Point out each Plasmodium parasite.
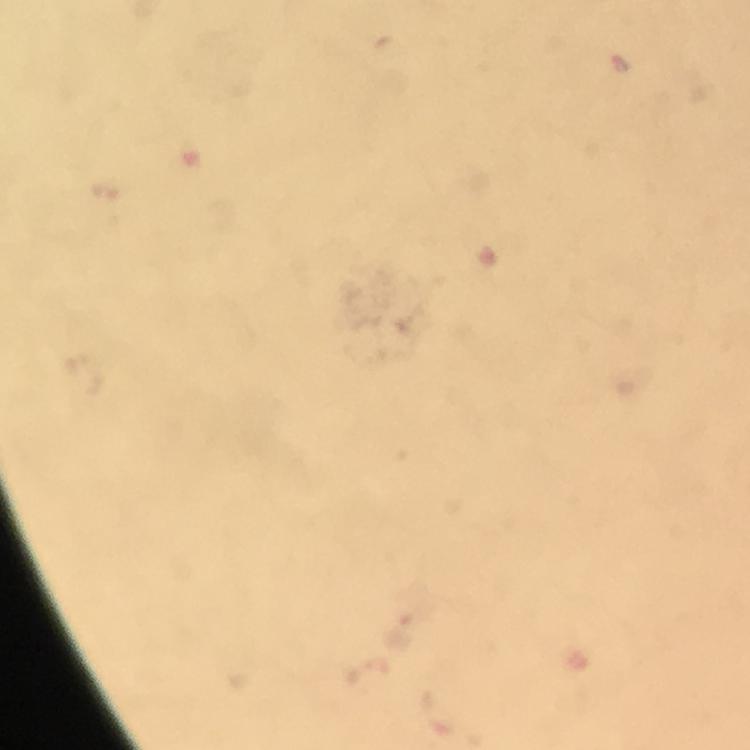

Approximate centers as {x, y} in pixels.
Plasmodium parasites: {619, 65}.

{
  "context": "from a diagnostic examination for malaria",
  "preparation": "thick blood smear",
  "immersion_oil": "used",
  "image_size": "750×750 pixels",
  "cropped_from": "a single field of view",
  "magnification": "100x",
  "capture": "smartphone camera through the microscope",
  "stain": "Giemsa"
}